Locate every uninfected red blood cell.
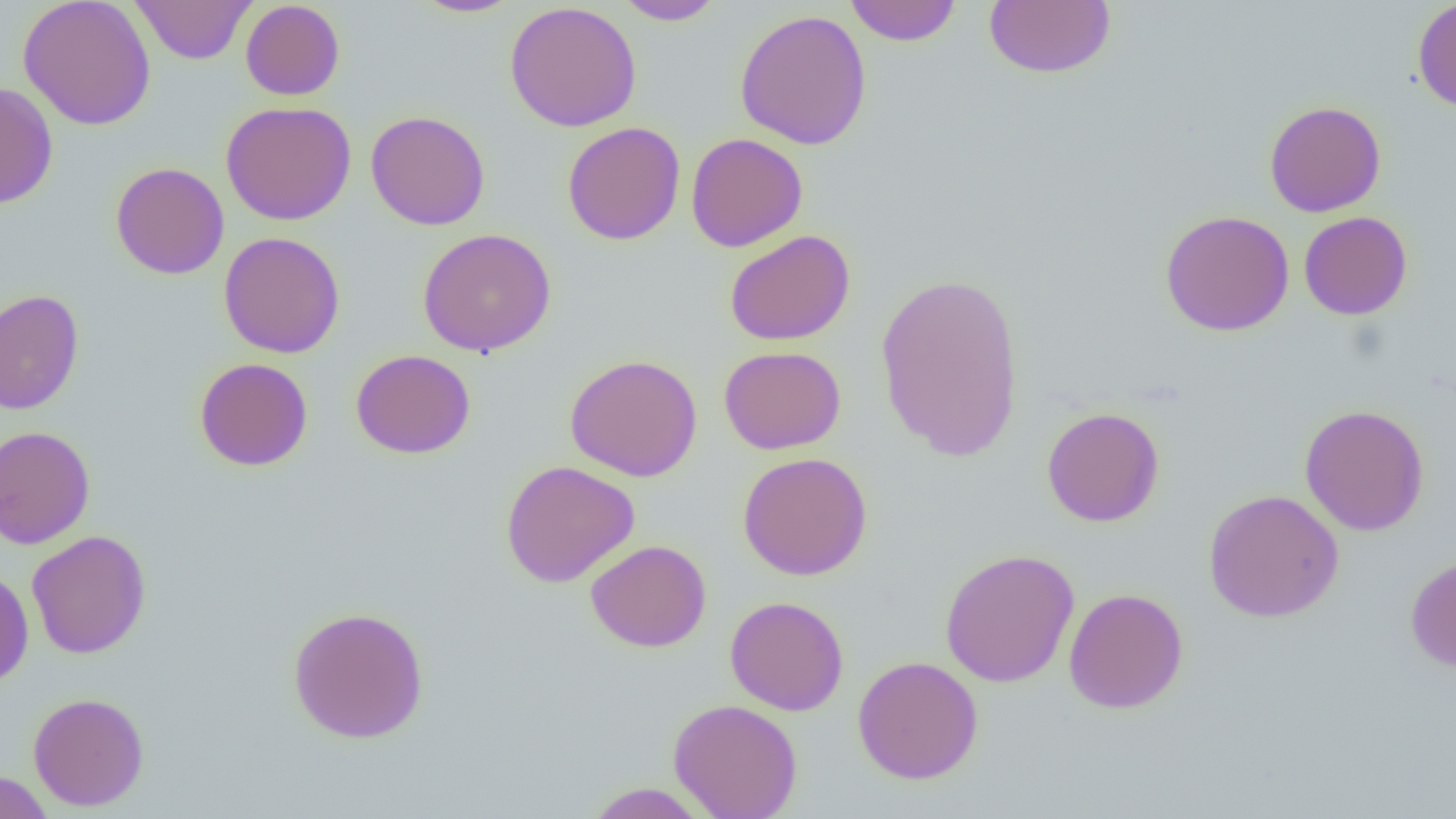

Approximate bounding boxes as (x1,y1)-(x2,y2) corner pairs in pixels.
Uninfected red blood cells: (18,0)-(157,130), (132,0)-(255,64), (411,0)-(522,18), (614,0)-(725,25), (844,0)-(962,46), (983,0)-(1116,80), (1412,0)-(1456,114), (240,1)-(345,100), (504,2)-(642,132), (734,9)-(873,150), (0,82)-(58,210), (1264,100)-(1386,217), (221,102)-(357,225), (365,110)-(490,230), (561,121)-(686,245), (685,132)-(808,252), (110,161)-(229,279), (1159,210)-(1295,336), (1298,211)-(1413,320), (417,228)-(557,357), (724,230)-(855,346), (218,231)-(345,359), (874,271)-(1026,463), (0,289)-(84,416), (719,345)-(846,455), (351,349)-(476,460), (565,354)-(703,482), (194,357)-(314,471), (1299,404)-(1430,536), (1041,406)-(1165,527), (0,426)-(96,549), (737,452)-(873,581), (500,460)-(640,587), (1203,488)-(1344,622), (26,530)-(151,659), (585,539)-(712,652), (939,548)-(1079,688), (1405,552)-(1456,672), (0,567)-(34,688), (1063,587)-(1189,713), (724,596)-(849,716), (287,605)-(430,744), (852,655)-(984,785), (27,692)-(149,811), (668,698)-(803,819), (0,769)-(54,819), (583,782)-(714,818).

Summary:
  - Slide-level diagnosis: negative for blood parasites
  - Image size: 1456×819 pixels
  - Magnification: 1000x
  - Field of view: single
  - Preparation: thin blood smear
  - Modality: optical microscopy